Assess this cell for malaria.
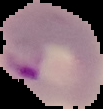

It is parasitized.

preparation = thin blood film
image type = cell region segmented out of the field of view; surrounding area masked to black
image size = 103×109 pixels